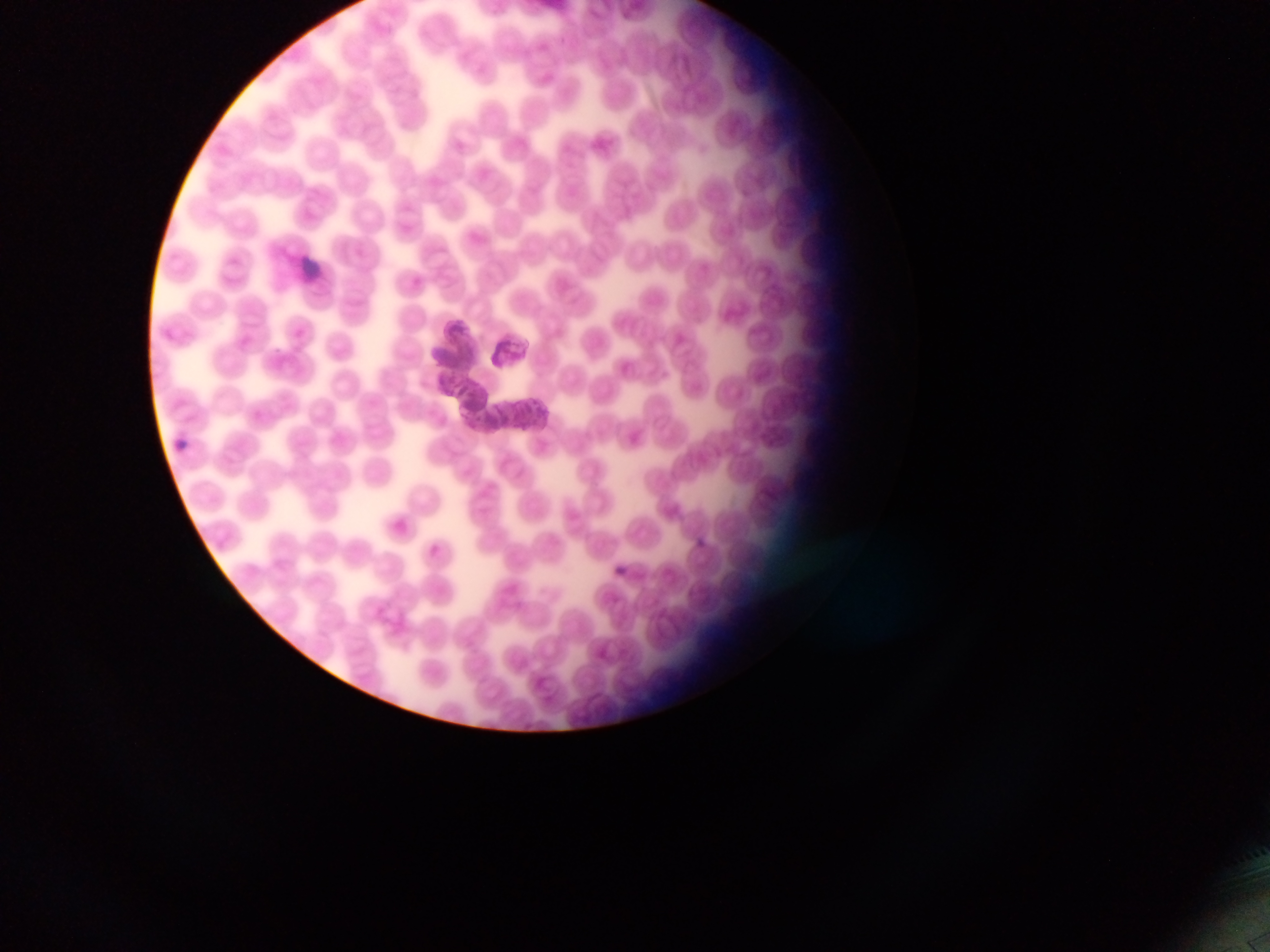

leukocyte locations = approximate bounding boxes as [left, top, right, bottom] in pixels: [296, 250, 326, 281]
malaria parasite locations = approximate bounding boxes as [left, top, right, bottom] in pixels: [471, 413, 487, 429]
capture = mobile-phone photograph through a microscope
image size = 1270×952 pixels
country = Ghana
field of view = single
preparation = thin blood smear